Assess the morphology of the red blood cells.
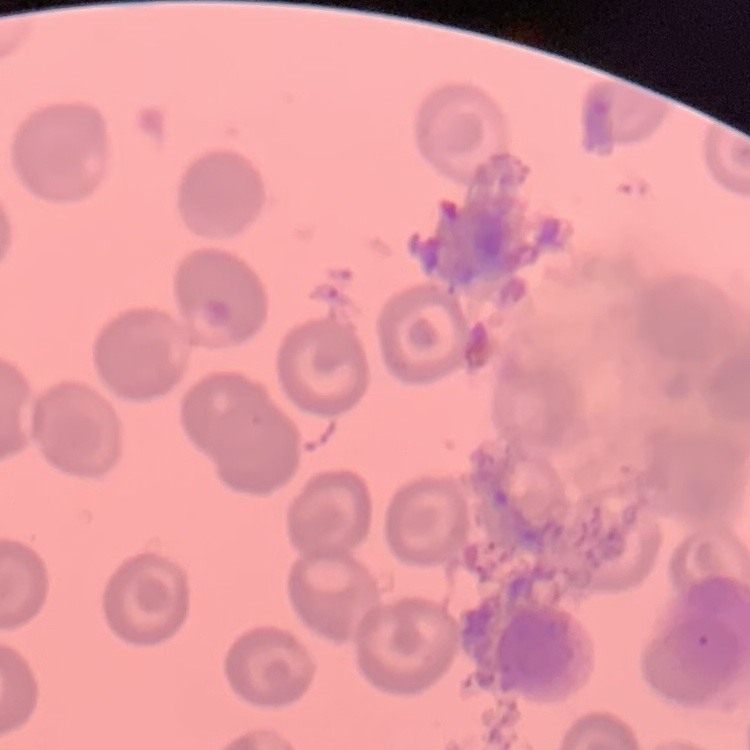

No rouleaux formation.

Summary:
  - Image type: square crop of a larger photomicrograph
  - Stain: Field's or Giemsa
  - Preparation: thin blood film